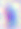 400x magnification. Toxoplasma gondii is seen. Micrograph.